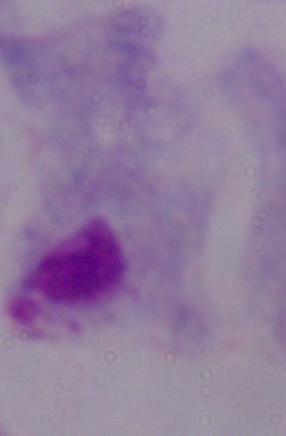
Summary:
  - Magnification: 1000x
  - Identification: trichomonad
  - Modality: photomicrograph